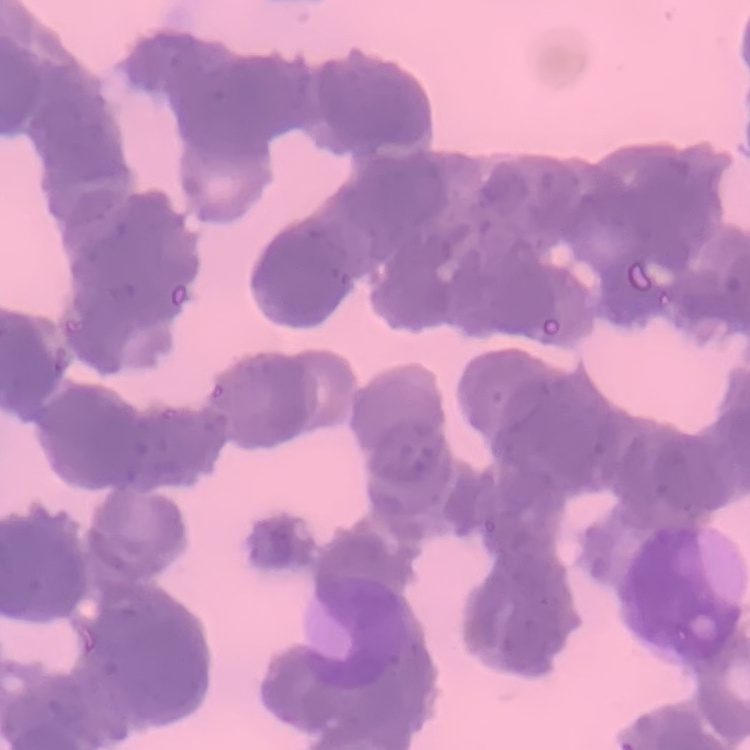

The erythrocytes show rouleaux formation. Thin peripheral smear. One tile cut from a larger photomicrograph. Field's or Giemsa stain.